Locate every malaria parasite.
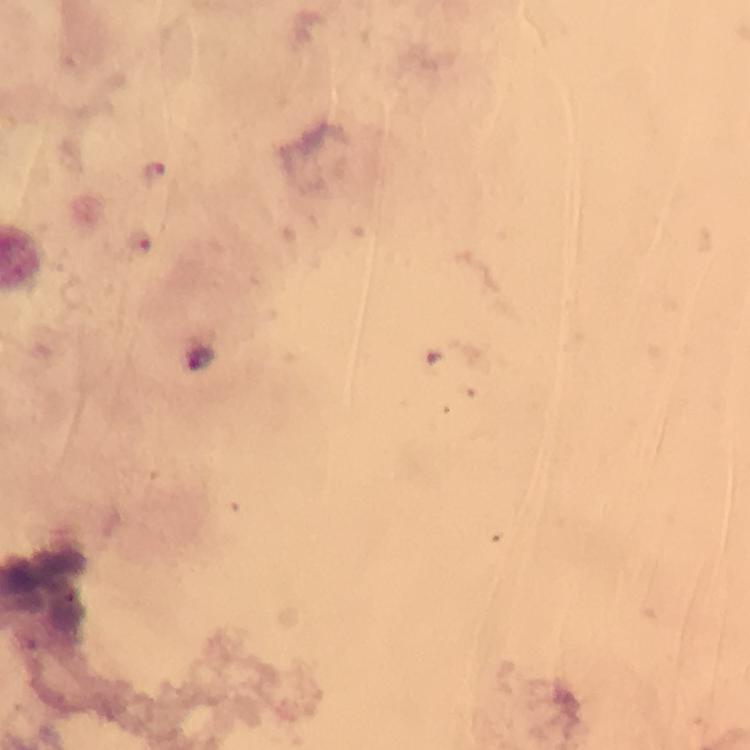
Approximate centers as {x, y} in pixels.
Malaria parasites: {156, 172}, {140, 239}, {199, 356}.

Immersion oil was used. Photographed through the microscope with a smartphone camera. Thick blood film. Giemsa stain. Image is 750×750 pixels. 100x magnification. Cropped region of a single field of view. From a diagnostic examination for malaria.